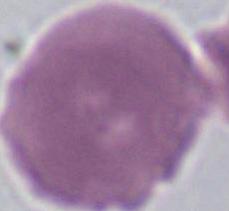

{
  "identification": "erythrocyte",
  "modality": "photomicrograph",
  "magnification": "1000x"
}